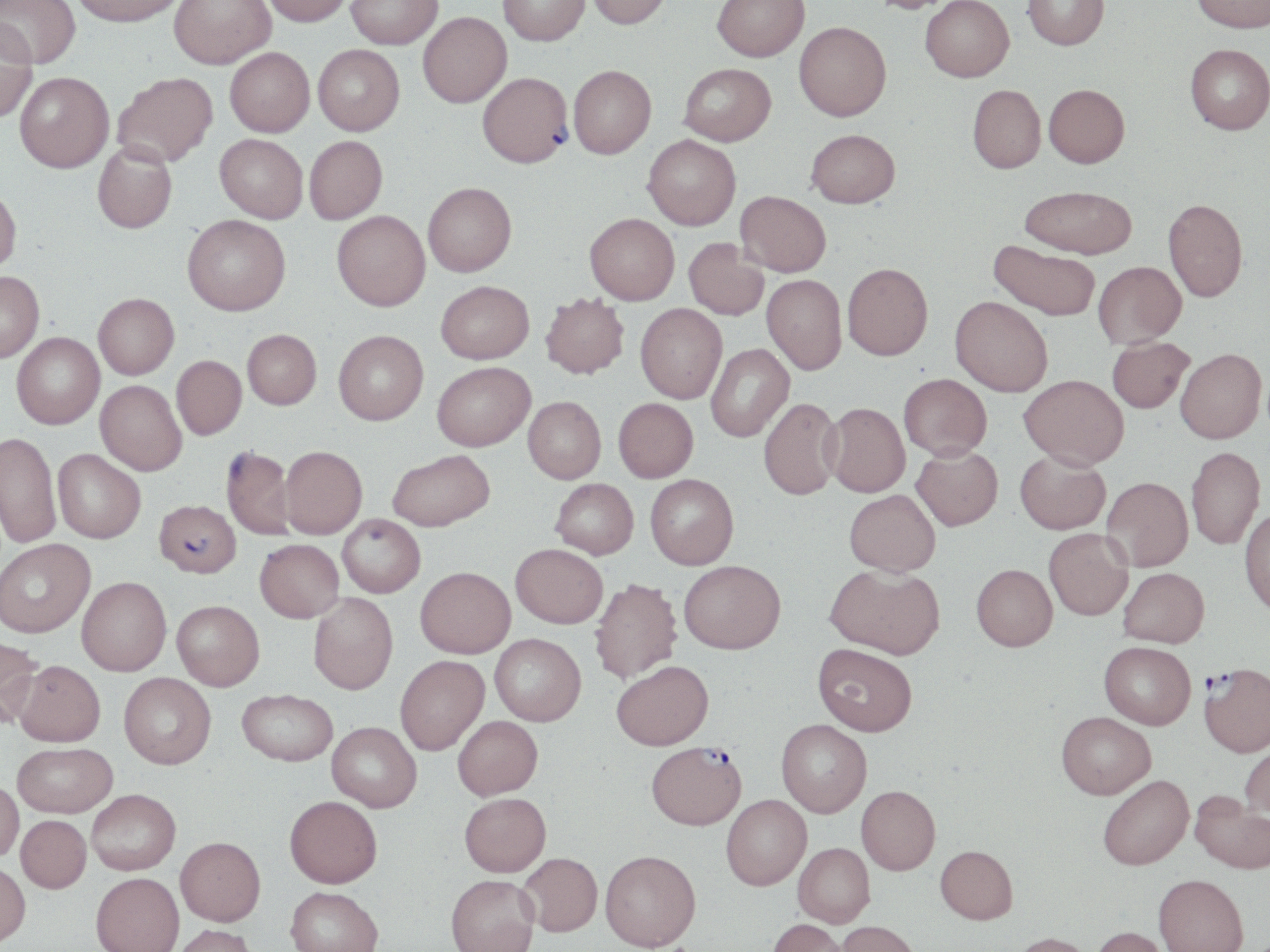
{
  "slide_level_diagnosis": "Plasmodium falciparum",
  "magnification": "1000x",
  "image_size": "1270×952 pixels",
  "plasmodium_falciparum_infected_red_blood_cell_locations": "approximate bounding boxes as named x1/y1/x2/y2 corners in pixels: (x1=477, y1=75, x2=573, y2=172), (x1=155, y1=499, x2=241, y2=578), (x1=1200, y1=664, x2=1270, y2=756), (x1=645, y1=740, x2=746, y2=829)",
  "stain": "May-Grünwald-Giemsa",
  "uninfected_red_blood_cell_locations": "approximate bounding boxes as named x1/y1/x2/y2 corners in pixels: (x1=0, y1=0, x2=80, y2=71), (x1=71, y1=0, x2=185, y2=31), (x1=169, y1=0, x2=276, y2=73), (x1=264, y1=0, x2=352, y2=30), (x1=346, y1=0, x2=442, y2=52), (x1=498, y1=0, x2=590, y2=49), (x1=587, y1=0, x2=672, y2=33), (x1=712, y1=0, x2=810, y2=65), (x1=867, y1=0, x2=957, y2=17), (x1=920, y1=0, x2=1014, y2=86), (x1=1023, y1=0, x2=1110, y2=54), (x1=1191, y1=0, x2=1269, y2=37), (x1=418, y1=15, x2=512, y2=111), (x1=0, y1=24, x2=38, y2=124), (x1=794, y1=26, x2=891, y2=125), (x1=312, y1=47, x2=405, y2=139), (x1=1185, y1=48, x2=1270, y2=138), (x1=225, y1=51, x2=315, y2=140), (x1=680, y1=67, x2=776, y2=148), (x1=569, y1=69, x2=656, y2=162), (x1=15, y1=75, x2=114, y2=177), (x1=113, y1=75, x2=218, y2=171), (x1=1044, y1=88, x2=1129, y2=172), (x1=967, y1=89, x2=1046, y2=176), (x1=806, y1=131, x2=900, y2=211), (x1=214, y1=136, x2=307, y2=225), (x1=642, y1=137, x2=740, y2=232), (x1=305, y1=138, x2=388, y2=226), (x1=92, y1=144, x2=177, y2=235), (x1=423, y1=185, x2=516, y2=279), (x1=0, y1=187, x2=21, y2=276), (x1=1018, y1=189, x2=1136, y2=260), (x1=735, y1=192, x2=831, y2=278), (x1=1162, y1=199, x2=1248, y2=303), (x1=331, y1=212, x2=431, y2=314), (x1=585, y1=215, x2=678, y2=306), (x1=183, y1=217, x2=290, y2=319), (x1=684, y1=239, x2=768, y2=321), (x1=988, y1=242, x2=1099, y2=323), (x1=1093, y1=262, x2=1186, y2=350), (x1=842, y1=264, x2=933, y2=363), (x1=0, y1=270, x2=44, y2=362), (x1=762, y1=276, x2=846, y2=377), (x1=436, y1=281, x2=534, y2=365), (x1=540, y1=293, x2=629, y2=380), (x1=93, y1=294, x2=179, y2=380), (x1=949, y1=299, x2=1052, y2=399), (x1=635, y1=304, x2=727, y2=405), (x1=243, y1=329, x2=321, y2=409), (x1=333, y1=331, x2=428, y2=426), (x1=12, y1=332, x2=105, y2=430), (x1=1107, y1=338, x2=1195, y2=414), (x1=706, y1=343, x2=795, y2=443), (x1=1176, y1=350, x2=1267, y2=445), (x1=172, y1=355, x2=247, y2=439), (x1=432, y1=362, x2=535, y2=451), (x1=899, y1=375, x2=992, y2=461), (x1=1019, y1=376, x2=1129, y2=472), (x1=95, y1=380, x2=186, y2=475), (x1=523, y1=396, x2=605, y2=483), (x1=613, y1=398, x2=698, y2=483), (x1=759, y1=398, x2=842, y2=500), (x1=822, y1=404, x2=909, y2=498), (x1=1, y1=431, x2=61, y2=548), (x1=221, y1=445, x2=296, y2=540), (x1=280, y1=446, x2=367, y2=538), (x1=911, y1=446, x2=1002, y2=531), (x1=1187, y1=447, x2=1265, y2=550), (x1=54, y1=448, x2=146, y2=543), (x1=387, y1=450, x2=495, y2=530), (x1=1015, y1=451, x2=1110, y2=535), (x1=645, y1=473, x2=739, y2=569), (x1=1101, y1=477, x2=1193, y2=572), (x1=550, y1=478, x2=638, y2=559), (x1=845, y1=489, x2=940, y2=577), (x1=1239, y1=508, x2=1270, y2=618), (x1=337, y1=513, x2=425, y2=597), (x1=1044, y1=528, x2=1133, y2=621), (x1=0, y1=538, x2=95, y2=637), (x1=255, y1=539, x2=344, y2=622), (x1=511, y1=543, x2=608, y2=627), (x1=679, y1=559, x2=787, y2=654), (x1=825, y1=564, x2=945, y2=659), (x1=972, y1=564, x2=1057, y2=651), (x1=416, y1=566, x2=515, y2=657), (x1=1118, y1=567, x2=1209, y2=648), (x1=77, y1=576, x2=171, y2=675), (x1=590, y1=578, x2=682, y2=683), (x1=309, y1=592, x2=398, y2=693), (x1=172, y1=600, x2=264, y2=690), (x1=490, y1=633, x2=586, y2=725), (x1=0, y1=635, x2=43, y2=727), (x1=1099, y1=641, x2=1195, y2=729), (x1=812, y1=643, x2=917, y2=735), (x1=395, y1=655, x2=489, y2=754), (x1=15, y1=660, x2=105, y2=746), (x1=612, y1=660, x2=713, y2=749), (x1=119, y1=672, x2=216, y2=768), (x1=237, y1=689, x2=337, y2=765), (x1=1055, y1=711, x2=1155, y2=799), (x1=453, y1=715, x2=542, y2=799), (x1=776, y1=719, x2=872, y2=817), (x1=327, y1=722, x2=421, y2=812), (x1=1240, y1=739, x2=1270, y2=821), (x1=12, y1=742, x2=116, y2=817), (x1=1098, y1=774, x2=1193, y2=870), (x1=0, y1=780, x2=23, y2=861), (x1=857, y1=785, x2=940, y2=874), (x1=87, y1=789, x2=180, y2=874), (x1=1190, y1=790, x2=1270, y2=873), (x1=459, y1=792, x2=551, y2=876), (x1=284, y1=795, x2=382, y2=887), (x1=721, y1=795, x2=811, y2=889), (x1=16, y1=815, x2=91, y2=893), (x1=175, y1=836, x2=265, y2=925), (x1=793, y1=842, x2=874, y2=927), (x1=935, y1=845, x2=1018, y2=923), (x1=600, y1=849, x2=701, y2=951), (x1=518, y1=852, x2=602, y2=936), (x1=0, y1=862, x2=30, y2=946), (x1=90, y1=872, x2=184, y2=952), (x1=1154, y1=873, x2=1248, y2=952), (x1=446, y1=874, x2=539, y2=952), (x1=285, y1=886, x2=384, y2=952), (x1=768, y1=918, x2=847, y2=952), (x1=836, y1=921, x2=922, y2=952), (x1=171, y1=924, x2=259, y2=952), (x1=1090, y1=926, x2=1171, y2=952), (x1=1010, y1=932, x2=1095, y2=952)",
  "modality": "optical microscopy",
  "preparation": "thin blood smear",
  "field_of_view": "single"
}